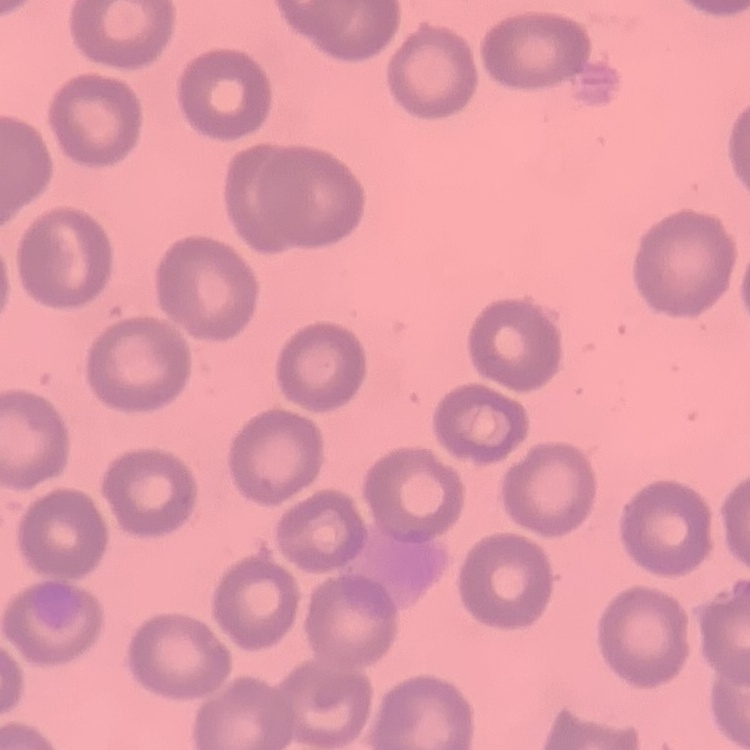
Summary:
  - Erythrocyte morphology: no rouleaux formation
  - Image type: one tile cut from a larger photomicrograph
  - Stain: Field's or Giemsa
  - Preparation: thin blood smear